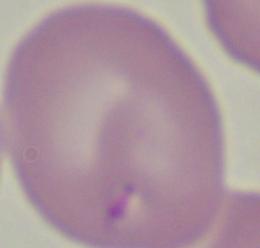

Summary:
  - Magnification: 1000x
  - Modality: photomicrograph
  - Identification: Babesia